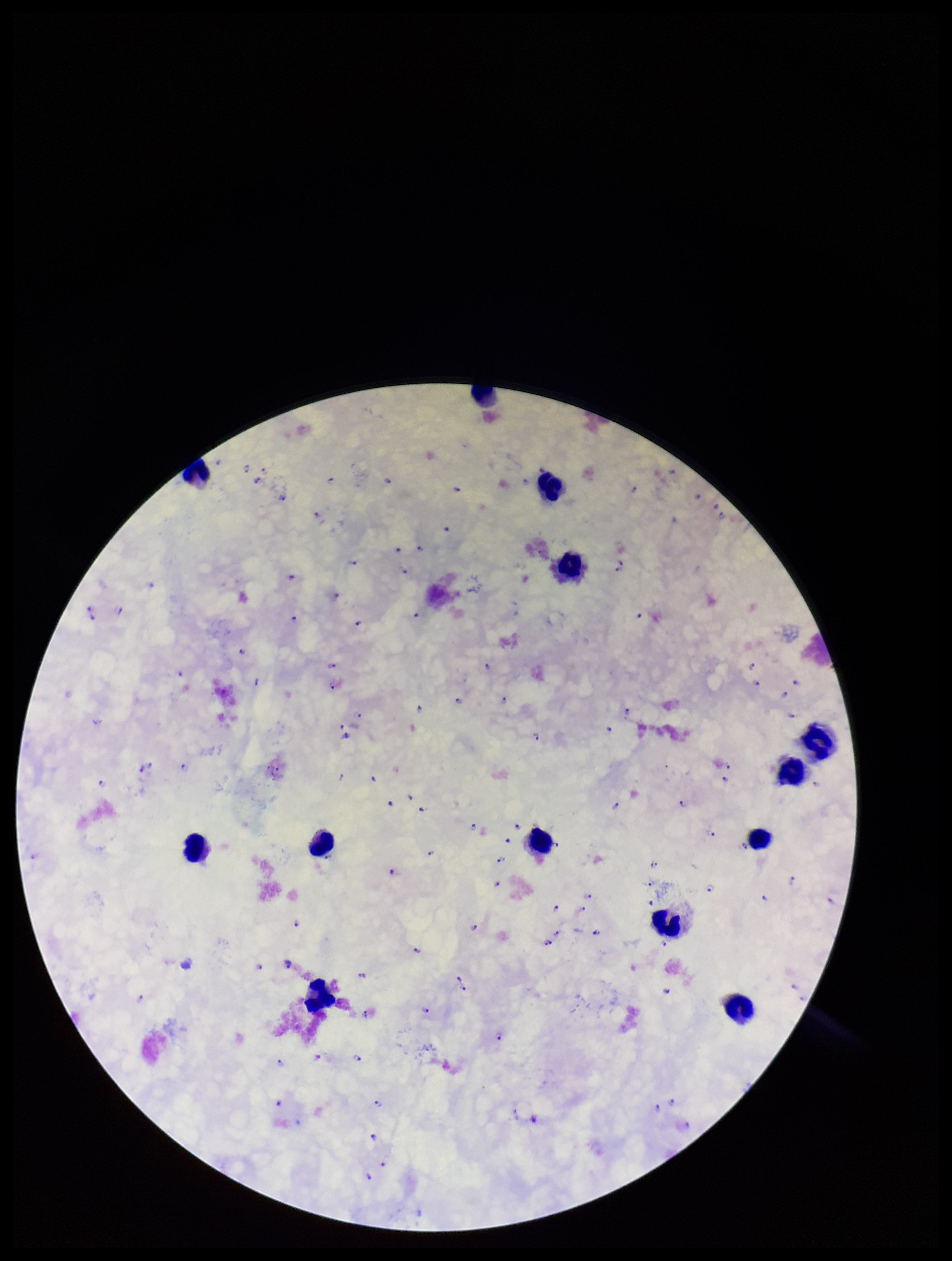
One field from this slide. Photographed through the microscope eyepiece with a smartphone camera. Parasite count: 110. Preparation: thick smear. Plasmodium parasites: seen. Giemsa stain. Patient malaria status: infected. Species reported for this patient: Plasmodium falciparum. Image is 952×1261 pixels. Leukocyte count: 13.